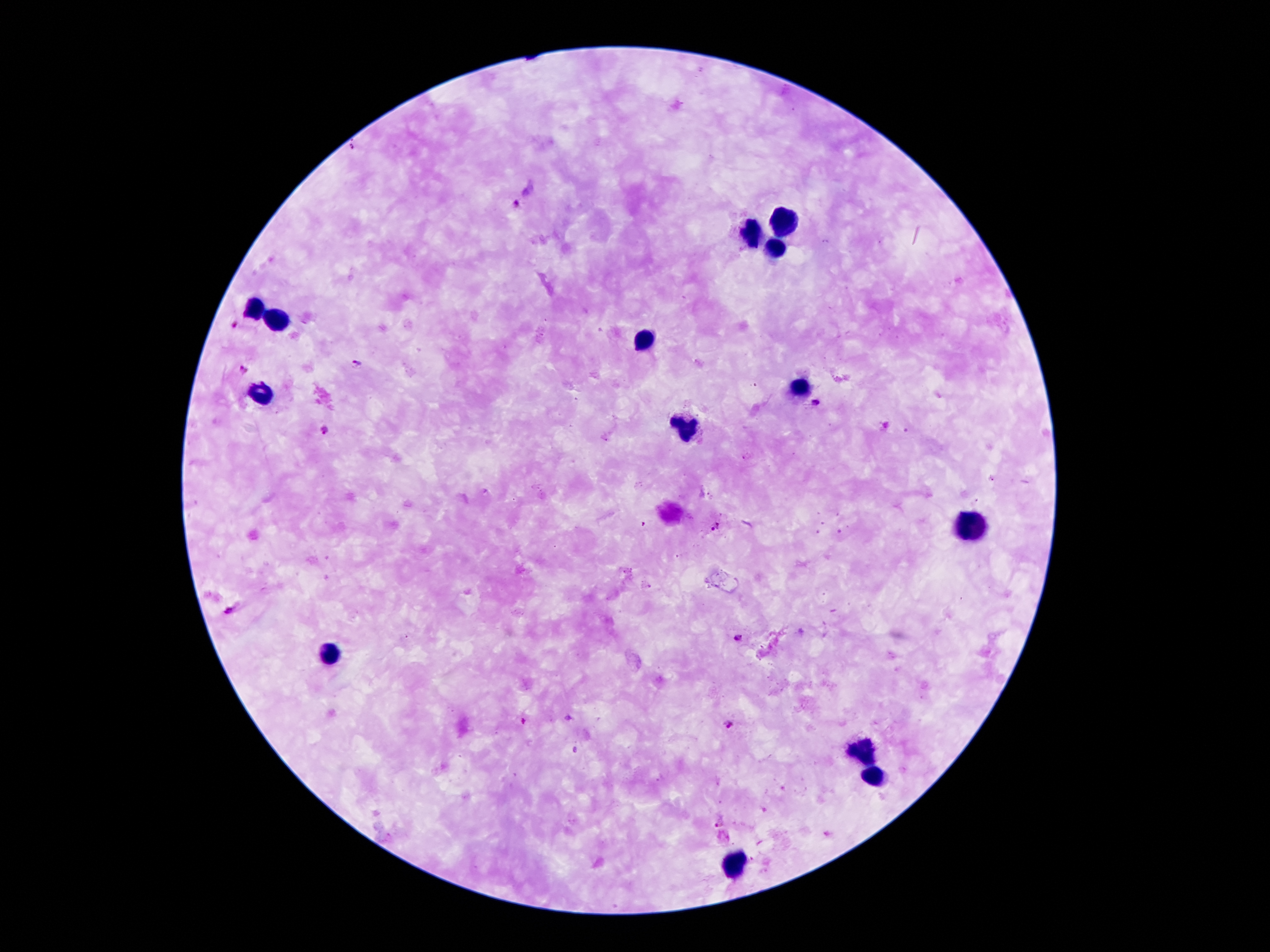
Approximate centers as {x, y} in pixels.
Summary:
  - Plasmodium parasite locations: {517, 203}, {235, 322}, {355, 362}, {242, 368}, {815, 403}, {324, 430}, {716, 526}, {229, 611}, {738, 638}, {523, 721}, {728, 724}, {719, 823}
  - Leukocyte locations: {784, 219}, {751, 232}, {777, 249}, {259, 306}, {280, 318}, {646, 339}, {800, 385}, {263, 390}, {689, 431}, {980, 531}, {331, 656}, {863, 748}, {874, 778}, {736, 863}
  - Stain: Giemsa
  - Field of view: one from this slide
  - Image size: 1270×952 pixels
  - Magnification: 100x
  - Patient malaria status: infected with Plasmodium falciparum
  - Preparation: thick blood film
  - Capture: smartphone through the microscope eyepiece